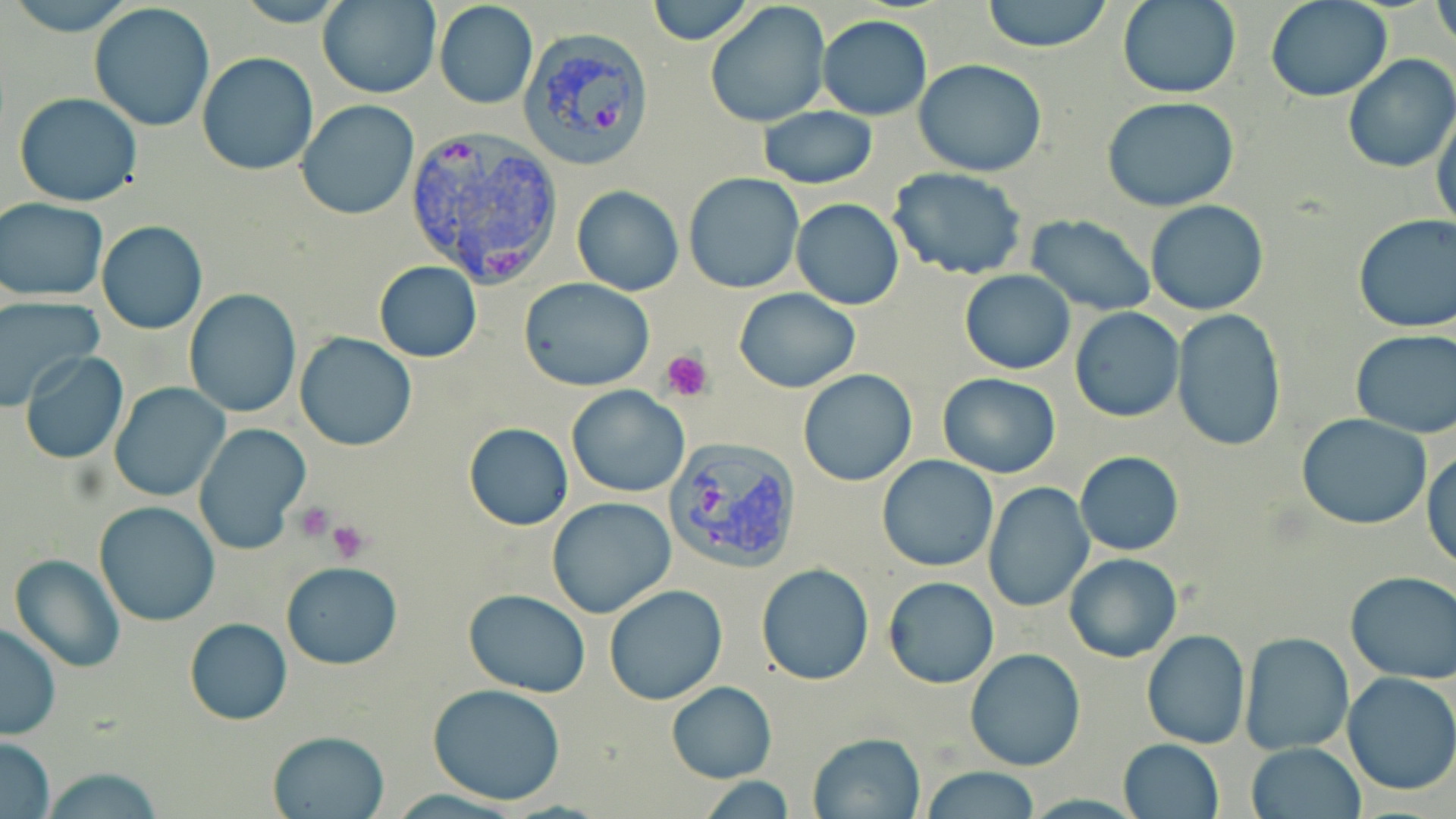

Summary:
  - Coordinate format: approximate bounding boxes as (x1,y1)-(x2,y2) corner pairs in pixels
  - Plasmodium vivax-infected red blood cell locations: (518,28)-(656,171), (403,130)-(565,286), (667,434)-(803,570)
  - Uninfected red blood cell locations: (7,0)-(134,32), (232,0)-(352,26), (319,0)-(438,98), (644,0)-(754,46), (981,0)-(1113,52), (1117,0)-(1239,99), (1433,0)-(1455,58), (432,1)-(538,109), (703,1)-(832,128), (1266,1)-(1393,101), (88,3)-(216,134), (818,14)-(932,120), (196,52)-(319,177), (1342,56)-(1456,174), (914,58)-(1047,176), (13,91)-(144,207), (1101,96)-(1241,212), (296,101)-(419,221), (1432,105)-(1456,232), (758,107)-(877,189), (887,166)-(1028,281), (682,172)-(805,294), (572,187)-(684,296), (1,197)-(108,302), (791,198)-(904,310), (1146,200)-(1269,315), (1353,213)-(1456,334), (1025,215)-(1157,315), (96,221)-(207,334), (373,260)-(482,363), (958,269)-(1074,375), (519,277)-(655,391), (733,287)-(860,393), (184,290)-(302,417), (0,297)-(102,411), (1069,308)-(1184,422), (1171,309)-(1287,451), (1349,329)-(1456,439), (295,332)-(418,452), (19,350)-(129,464), (798,368)-(918,487), (938,372)-(1061,478), (109,383)-(230,502), (567,386)-(690,497), (1297,414)-(1434,531), (464,423)-(573,530), (192,424)-(311,556), (1424,450)-(1456,571), (1075,451)-(1184,556), (876,454)-(999,572), (984,481)-(1095,613), (546,496)-(677,619), (94,501)-(220,627), (1063,552)-(1182,662), (8,554)-(126,673), (283,561)-(402,670), (756,564)-(874,685), (1345,572)-(1456,682), (882,575)-(1000,689), (603,584)-(727,703), (464,589)-(590,697), (183,617)-(293,725), (0,624)-(60,739), (1140,629)-(1250,750), (1239,632)-(1355,755), (964,648)-(1086,770), (1343,673)-(1456,795), (665,682)-(778,783), (426,684)-(568,805), (268,729)-(389,818), (808,733)-(923,818), (0,736)-(55,818), (1117,738)-(1224,819), (1246,742)-(1365,819), (923,766)-(1041,819), (36,767)-(165,818), (701,777)-(799,816)
  - Platelet locations: (660,350)-(713,400), (293,502)-(334,542), (328,519)-(371,563)
  - Slide-level diagnosis: Plasmodium vivax
  - Preparation: thin blood film
  - Stain: May-Grünwald-Giemsa
  - Modality: optical microscopy
  - Field of view: single
  - Image size: 1456×819 pixels
  - Magnification: 1000x